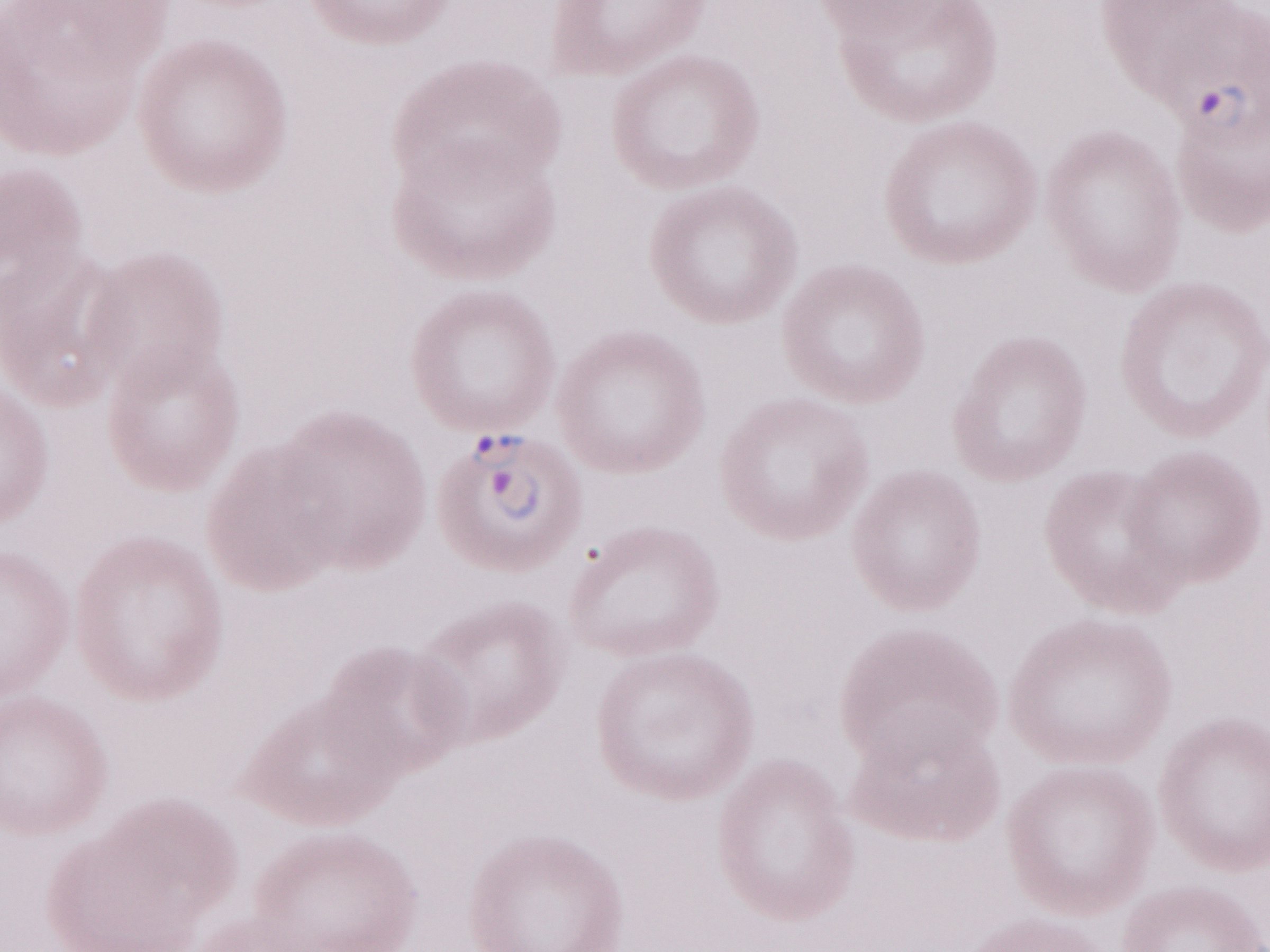 Thin blood smear. May-Grünwald-Giemsa-stained preparation. Patient diagnosis: malaria infection. Image is 1270×952 pixels. Magnification: 1,000x. One field of this slide. Olympus BX43 microscope, Olympus DP73 camera.